Assess this cell for malaria.
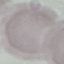
Uninfected.

{
  "capture": "smartphone camera at the microscope eyepiece",
  "stain": "Giemsa",
  "preparation": "thin blood film",
  "image_type": "cell patch, automatically extracted from a larger field of view and resized to 64 × 64 pixels"
}